Locate every Plasmodium falciparum-infected red blood cell.
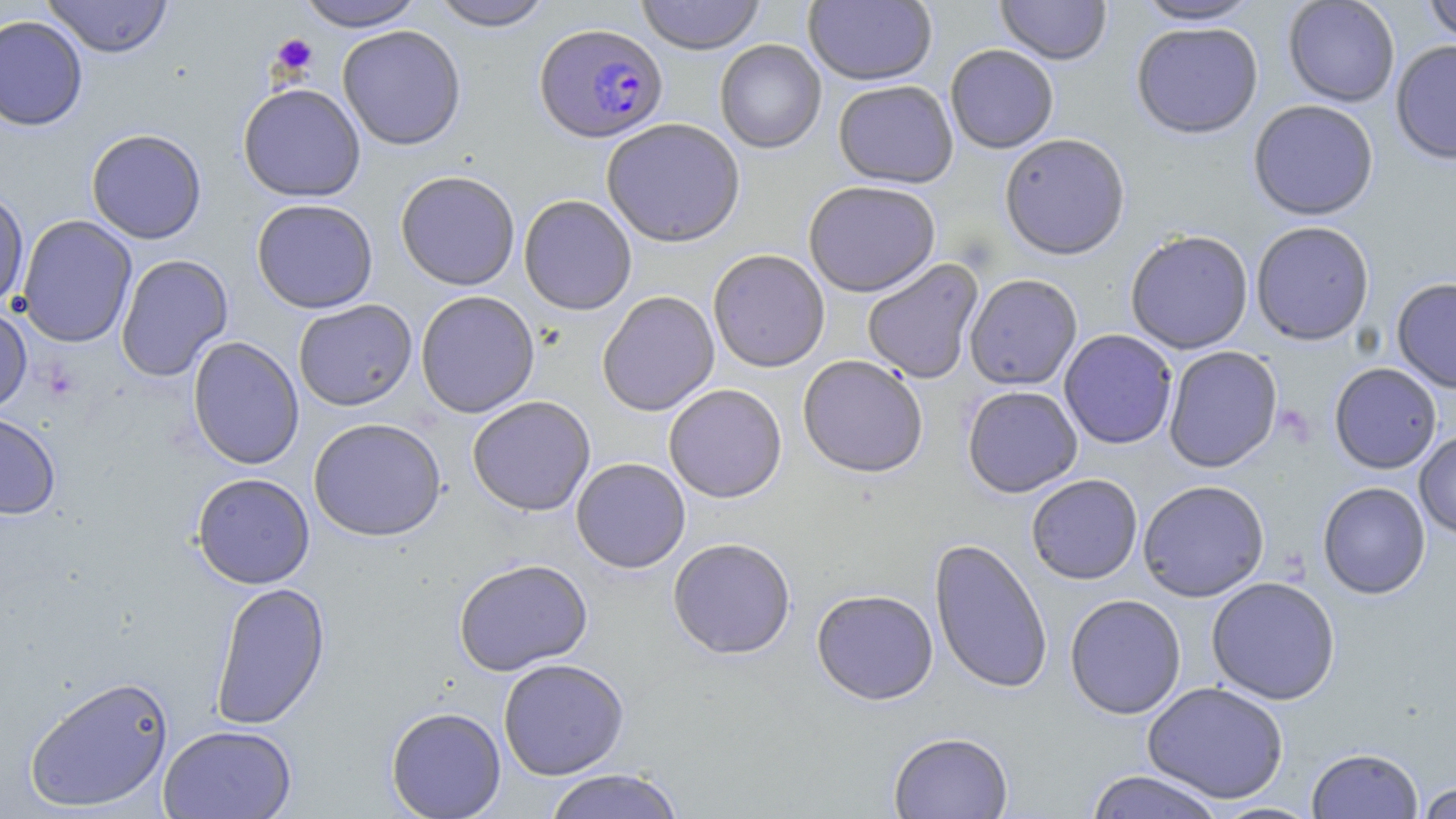

Approximate bounding boxes as (x1,y1)-(x2,y2) corner pairs in pixels.
Plasmodium falciparum-infected red blood cells: (534,23)-(668,142).

Platelet locations: (271,34)-(318,75). Uninfected red blood cell locations: (42,0)-(173,58), (295,0)-(428,31), (429,0)-(553,31), (635,0)-(765,55), (804,0)-(937,86), (995,0)-(1111,65), (1134,0)-(1262,25), (1283,0)-(1400,107), (1421,0)-(1456,43), (0,15)-(88,131), (1131,21)-(1263,139), (337,25)-(466,150), (715,39)-(826,153), (1390,40)-(1456,165), (945,44)-(1059,153), (833,80)-(958,188), (238,83)-(366,202), (1248,99)-(1379,221), (601,118)-(745,247), (86,128)-(207,244), (999,132)-(1130,259), (395,170)-(521,290), (803,180)-(940,297), (0,188)-(29,309), (518,195)-(637,315), (251,198)-(378,314), (17,215)-(137,348), (1250,221)-(1375,345), (1125,229)-(1254,354), (708,249)-(830,372), (116,254)-(233,382), (862,259)-(984,383), (964,273)-(1083,390), (1391,277)-(1456,394), (415,290)-(540,418), (597,291)-(720,416), (293,299)-(417,411), (0,303)-(32,418), (1059,329)-(1178,449), (187,336)-(304,470), (1163,346)-(1283,472), (798,355)-(928,478), (1329,362)-(1442,474), (663,383)-(787,503), (962,385)-(1083,497), (467,395)-(596,516), (0,412)-(61,520), (308,417)-(446,541), (1414,430)-(1456,539), (571,458)-(690,573), (192,472)-(315,589), (1026,474)-(1143,584), (1137,479)-(1270,602), (1317,481)-(1430,599), (668,537)-(796,659), (929,538)-(1053,694), (453,558)-(592,676), (1206,576)-(1341,705), (210,581)-(330,730), (812,589)-(938,704), (1065,593)-(1186,719), (498,658)-(629,779), (24,674)-(174,813), (1142,681)-(1289,804), (386,706)-(507,819), (158,724)-(297,819), (888,731)-(1014,819), (1306,746)-(1423,818), (543,768)-(686,819), (1084,770)-(1225,819), (1416,781)-(1456,819). Slide-level diagnosis: Plasmodium falciparum. Image is 1456×819 pixels. Thin blood smear. Captured at 1000x magnification. Single field of view. May-Grünwald-Giemsa-stained preparation. Light microscopy.